Classify this cell by malaria status.
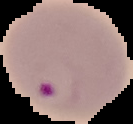
Parasitized.

Image is 133×124 pixels. From a thin blood smear. The area outside the segmented cell region is set to black.